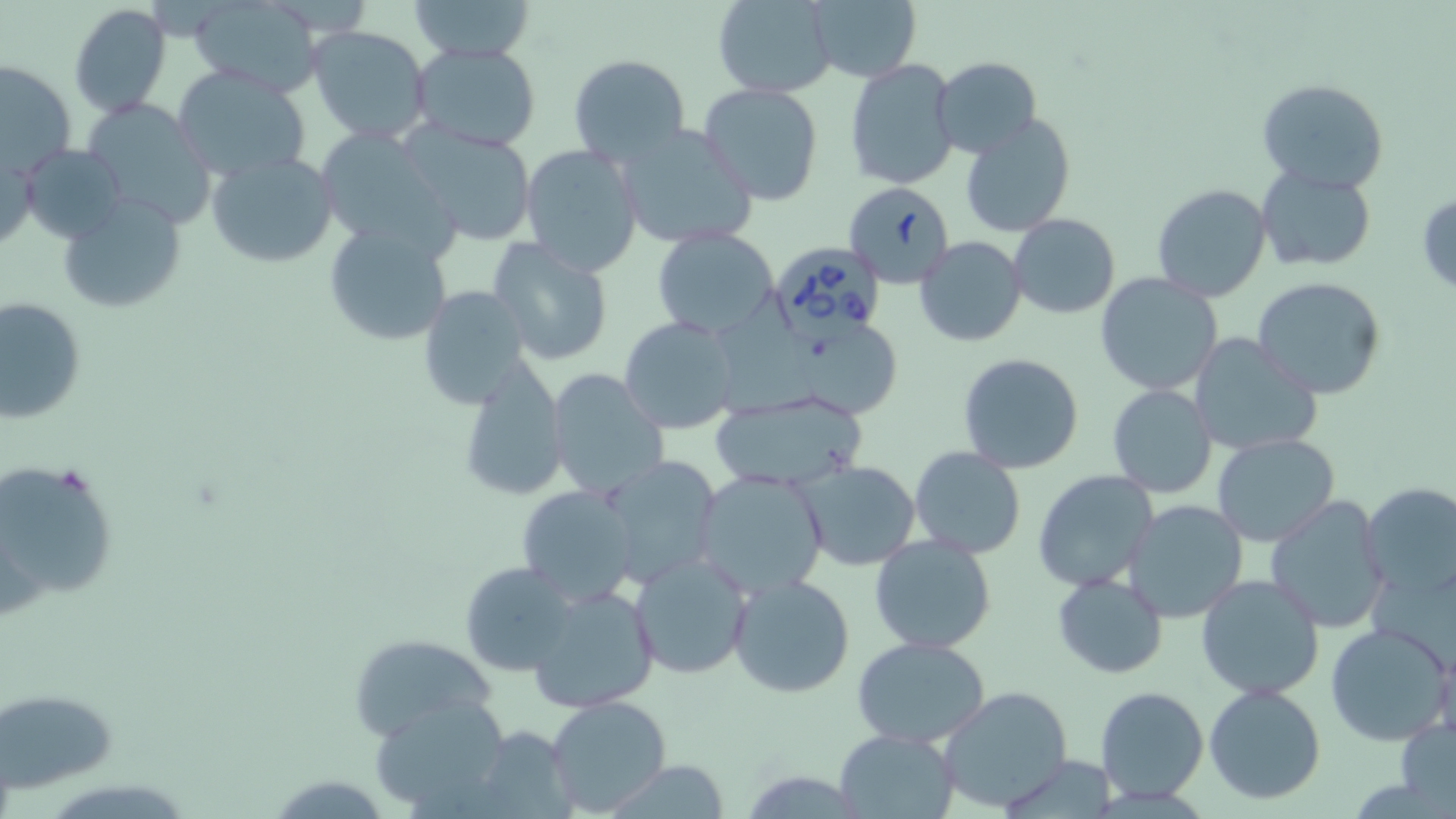

Summary:
  - Coordinate format: approximate bounding boxes as (x1, y1, x2, y2) in pixels
  - Babesia divergens-infected red blood cell locations: (842, 180, 953, 288), (769, 240, 891, 343)
  - Uninfected red blood cell locations: (406, 0, 536, 61), (713, 0, 838, 98), (805, 0, 921, 83), (68, 3, 172, 116), (187, 3, 325, 92), (309, 26, 432, 143), (410, 42, 543, 152), (568, 52, 691, 166), (933, 56, 1042, 158), (845, 58, 959, 190), (2, 61, 74, 177), (172, 64, 311, 182), (1255, 77, 1390, 195), (698, 82, 823, 207), (80, 98, 219, 231), (958, 113, 1077, 238), (396, 120, 540, 247), (614, 122, 761, 250), (312, 129, 460, 257), (21, 144, 130, 246), (519, 144, 644, 276), (0, 152, 41, 254), (208, 152, 339, 269), (1256, 166, 1378, 271), (1150, 182, 1273, 301), (1416, 190, 1456, 297), (57, 195, 187, 313), (1008, 215, 1121, 319), (322, 221, 454, 347), (651, 227, 781, 341), (486, 235, 615, 368), (915, 236, 1027, 348), (1095, 272, 1223, 395), (1250, 276, 1390, 401), (417, 285, 532, 408), (0, 297, 86, 423), (713, 298, 818, 426), (619, 315, 741, 435), (798, 328, 900, 421), (1190, 334, 1323, 456), (957, 354, 1086, 474), (457, 357, 569, 503), (546, 367, 671, 501), (1106, 383, 1218, 498), (708, 394, 867, 493), (1213, 434, 1340, 546), (908, 446, 1026, 559), (600, 456, 721, 588), (1, 460, 120, 610), (793, 460, 922, 572), (693, 469, 829, 599), (1032, 471, 1159, 592), (1358, 480, 1456, 600), (516, 483, 639, 606), (1265, 494, 1392, 634), (1123, 499, 1247, 623), (867, 532, 997, 655), (627, 551, 753, 680), (459, 559, 582, 675), (1052, 572, 1169, 678), (729, 574, 855, 697), (1196, 574, 1326, 702), (527, 582, 661, 714), (1324, 623, 1455, 747), (345, 634, 498, 740), (852, 637, 991, 748), (1203, 684, 1326, 804), (938, 685, 1075, 813), (1096, 686, 1208, 802), (3, 687, 118, 794), (370, 694, 513, 814), (545, 695, 673, 817), (1395, 719, 1456, 813), (834, 729, 956, 817), (996, 755, 1120, 818), (599, 761, 735, 817)
  - Slide-level diagnosis: Babesia divergens
  - Image size: 1456×819 pixels
  - Field of view: one of a larger specimen
  - Modality: optical microscopy
  - Magnification: 1000x
  - Stain: May-Grünwald-Giemsa
  - Preparation: thin blood film